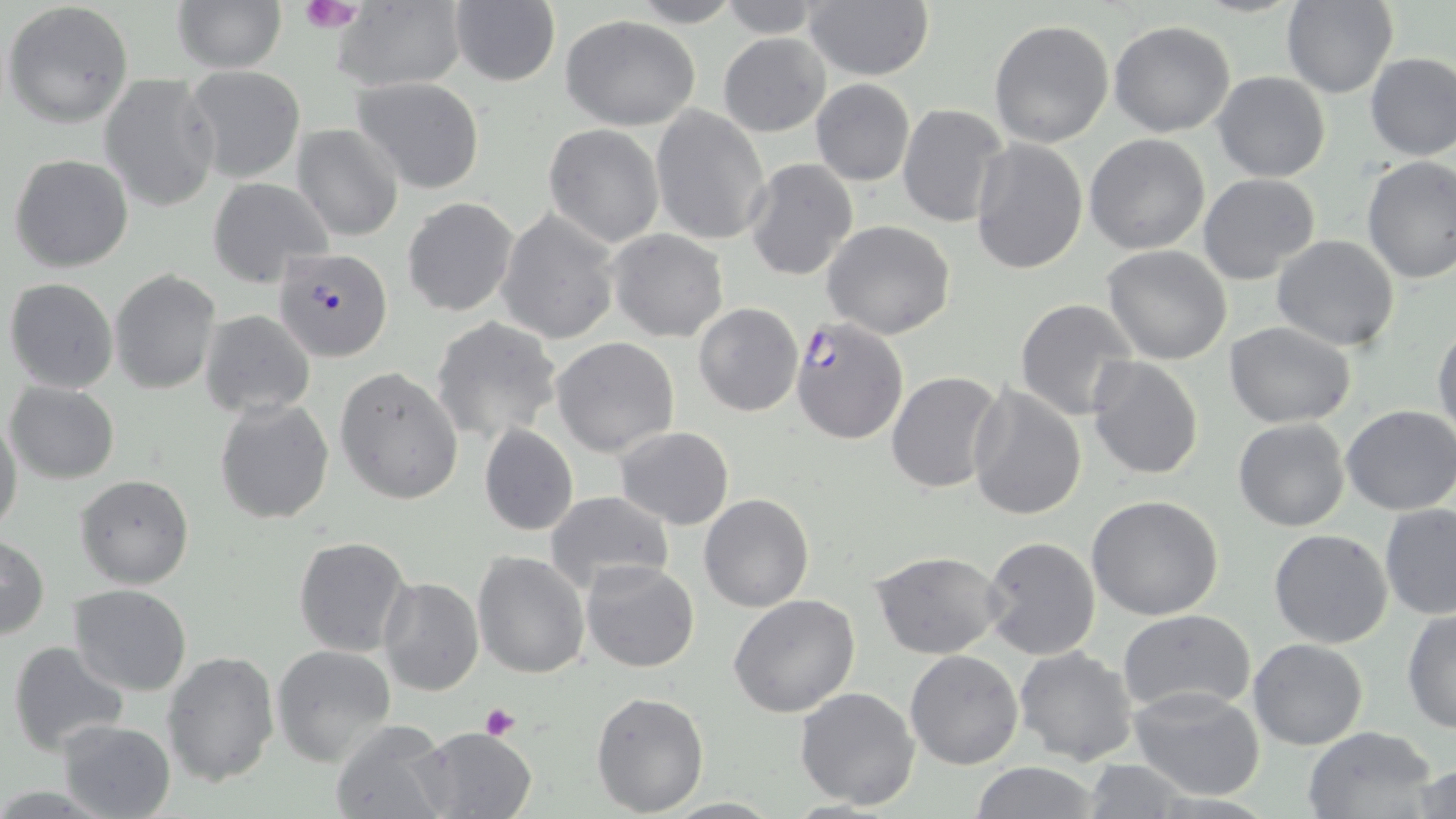

Approximate bounding boxes as [x1, y1, x2, y2] in pixels. Uninfected red blood cell locations: [172, 0, 286, 73], [448, 0, 561, 88], [628, 0, 746, 28], [716, 0, 826, 38], [802, 0, 934, 81], [1282, 0, 1396, 98], [2, 2, 134, 128], [332, 4, 464, 89], [561, 16, 700, 130], [988, 19, 1115, 147], [1109, 20, 1236, 136], [718, 33, 830, 137], [1364, 51, 1456, 160], [185, 65, 306, 182], [1211, 71, 1330, 182], [98, 73, 221, 214], [353, 75, 486, 194], [809, 78, 914, 186], [897, 103, 1009, 228], [651, 106, 771, 246], [293, 123, 404, 242], [543, 124, 665, 248], [1084, 133, 1211, 254], [969, 138, 1089, 274], [9, 152, 134, 273], [1360, 155, 1456, 284], [743, 158, 858, 281], [1197, 173, 1321, 284], [207, 178, 333, 287], [402, 198, 518, 317], [496, 210, 620, 345], [823, 220, 954, 338], [606, 230, 729, 342], [1271, 233, 1399, 352], [1102, 245, 1234, 365], [110, 269, 222, 395], [4, 277, 119, 393], [1015, 299, 1140, 422], [693, 302, 805, 416], [200, 308, 315, 417], [431, 316, 562, 445], [1226, 320, 1356, 427], [1431, 322, 1455, 443], [551, 336, 679, 457], [1086, 355, 1205, 479], [334, 366, 464, 505], [886, 371, 1003, 494], [6, 381, 120, 484], [967, 383, 1088, 521], [214, 397, 334, 525], [1342, 404, 1456, 517], [0, 410, 23, 538], [1232, 418, 1351, 532], [479, 424, 579, 536], [614, 426, 736, 529], [76, 474, 195, 590], [544, 489, 674, 595], [699, 492, 814, 612], [1085, 495, 1225, 621], [1379, 505, 1456, 620], [1268, 528, 1393, 648], [0, 533, 50, 640], [979, 535, 1104, 660], [293, 536, 412, 656], [870, 548, 1005, 659], [472, 551, 591, 679], [580, 559, 701, 672], [378, 576, 484, 695], [68, 583, 195, 697], [728, 595, 861, 718], [1117, 610, 1256, 717], [1402, 611, 1456, 734], [1247, 639, 1368, 751], [8, 641, 129, 757], [271, 644, 396, 765], [1013, 647, 1139, 766], [161, 649, 281, 787], [904, 650, 1024, 769], [798, 670, 1020, 792], [795, 685, 922, 810], [1129, 685, 1267, 799], [591, 689, 709, 814], [58, 719, 176, 818], [331, 719, 452, 818], [418, 727, 537, 818], [1302, 727, 1440, 819], [1080, 760, 1198, 818], [968, 762, 1104, 819], [1410, 763, 1456, 816]. Plasmodium falciparum-infected red blood cell locations: [275, 247, 391, 360], [791, 317, 908, 444]. Platelet locations: [298, 0, 362, 30], [479, 703, 522, 740]. Slide-level diagnosis: Plasmodium falciparum. Light microscopy. Image is 1456×819 pixels. 1000x magnification. May-Grünwald-Giemsa stain. Thin blood smear. Single field of view.